Identify the parasite.
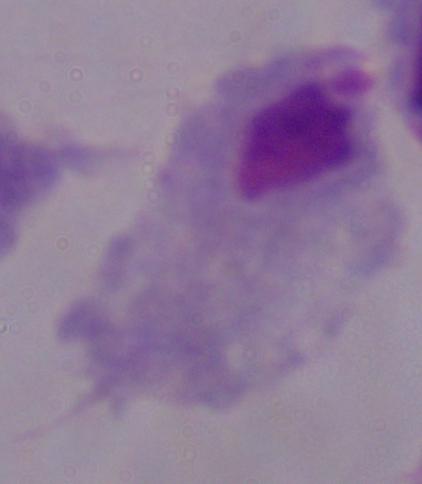

This is a trichomonad.

magnification: 1000x
modality: micrograph